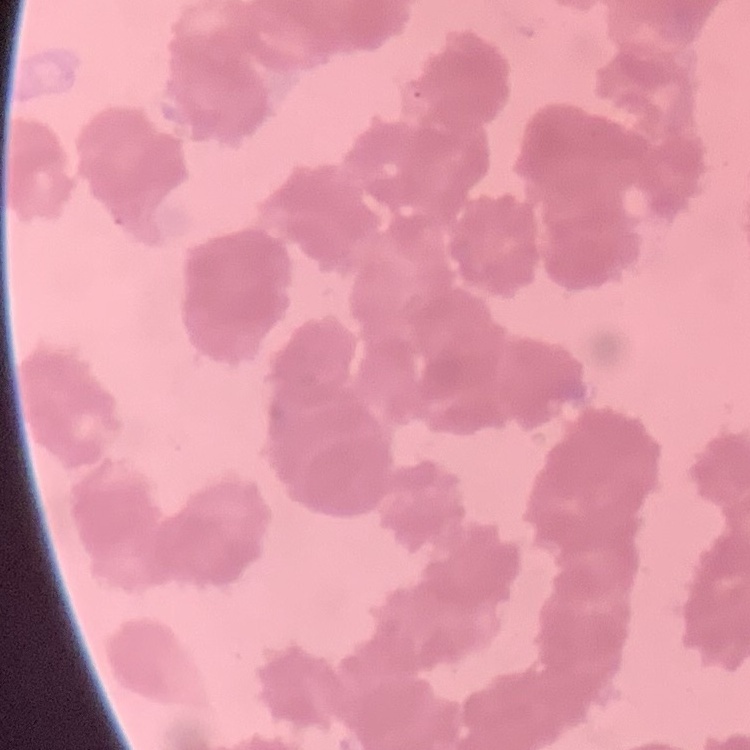 The red blood cells show rouleaux formation. Thin blood smear. Field's or Giemsa stain. Square crop of a larger photomicrograph.